Classify this cell by malaria status.
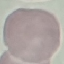
Uninfected.

Summary:
  - Image type: automatically extracted cell patch, resized to 64 × 64 pixels
  - Stain: Giemsa
  - Capture: smartphone camera at the microscope eyepiece
  - Preparation: thin smear